Point out each leukocyte.
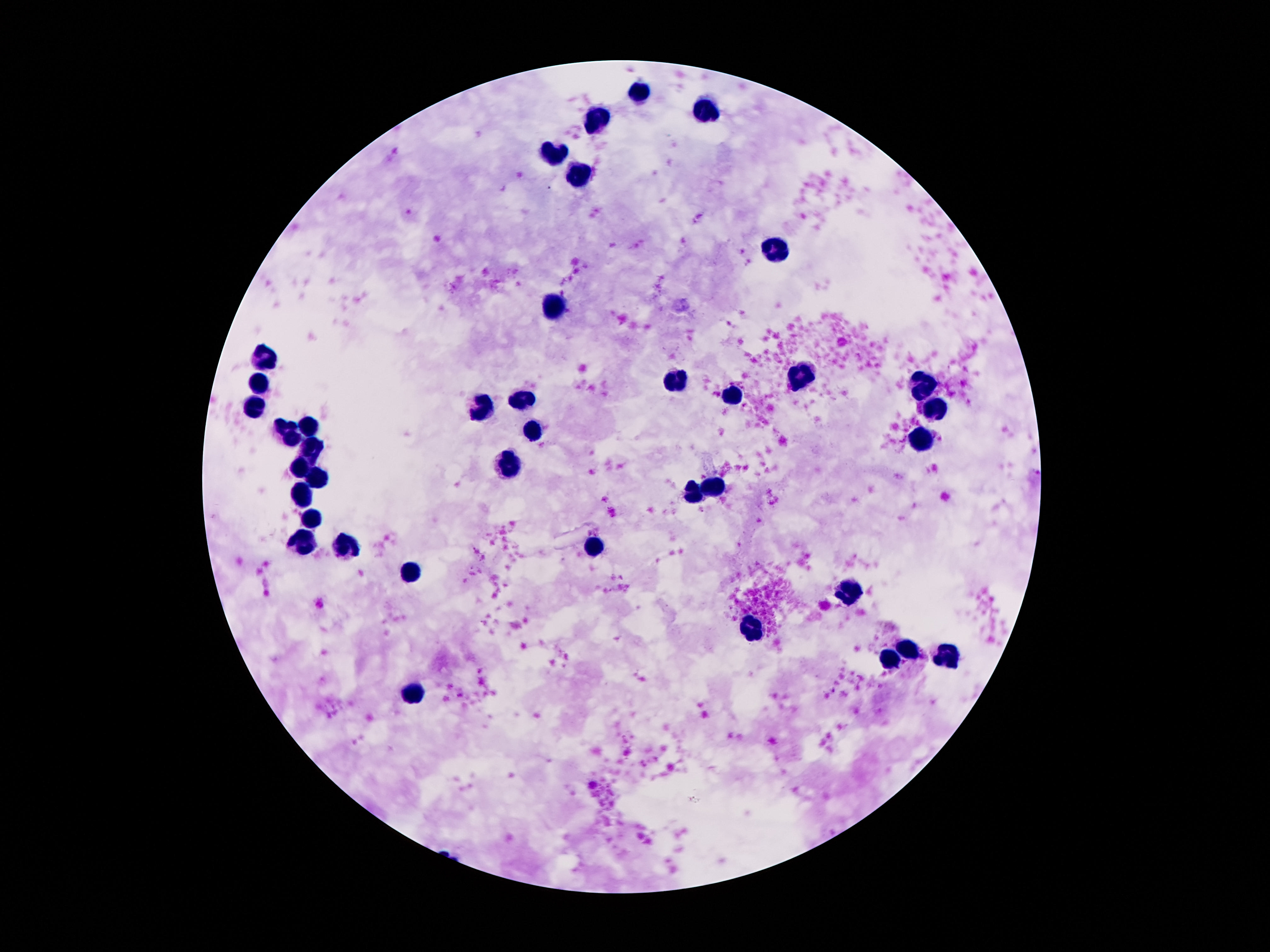

Approximate object centers, in pixels from the top-left corner.
Leukocytes: (x=638, y=90), (x=705, y=107), (x=598, y=117), (x=554, y=155), (x=579, y=172), (x=778, y=253), (x=554, y=305), (x=268, y=351), (x=260, y=380), (x=678, y=380), (x=801, y=380), (x=923, y=386), (x=734, y=392), (x=526, y=399), (x=251, y=405), (x=484, y=408), (x=938, y=410), (x=304, y=426), (x=287, y=432), (x=533, y=436), (x=921, y=440), (x=312, y=451), (x=510, y=464), (x=302, y=470), (x=316, y=480), (x=715, y=485), (x=692, y=491), (x=302, y=499), (x=312, y=520), (x=304, y=541), (x=346, y=550), (x=592, y=551), (x=413, y=569), (x=848, y=595), (x=755, y=628), (x=911, y=649), (x=951, y=657), (x=888, y=659), (x=415, y=691).

Single field of view. Image is 1270×952 pixels. Patient malaria status: negative. Giemsa-stained preparation. Smartphone photograph taken through the microscope eyepiece. Thick blood film. 100x magnification.